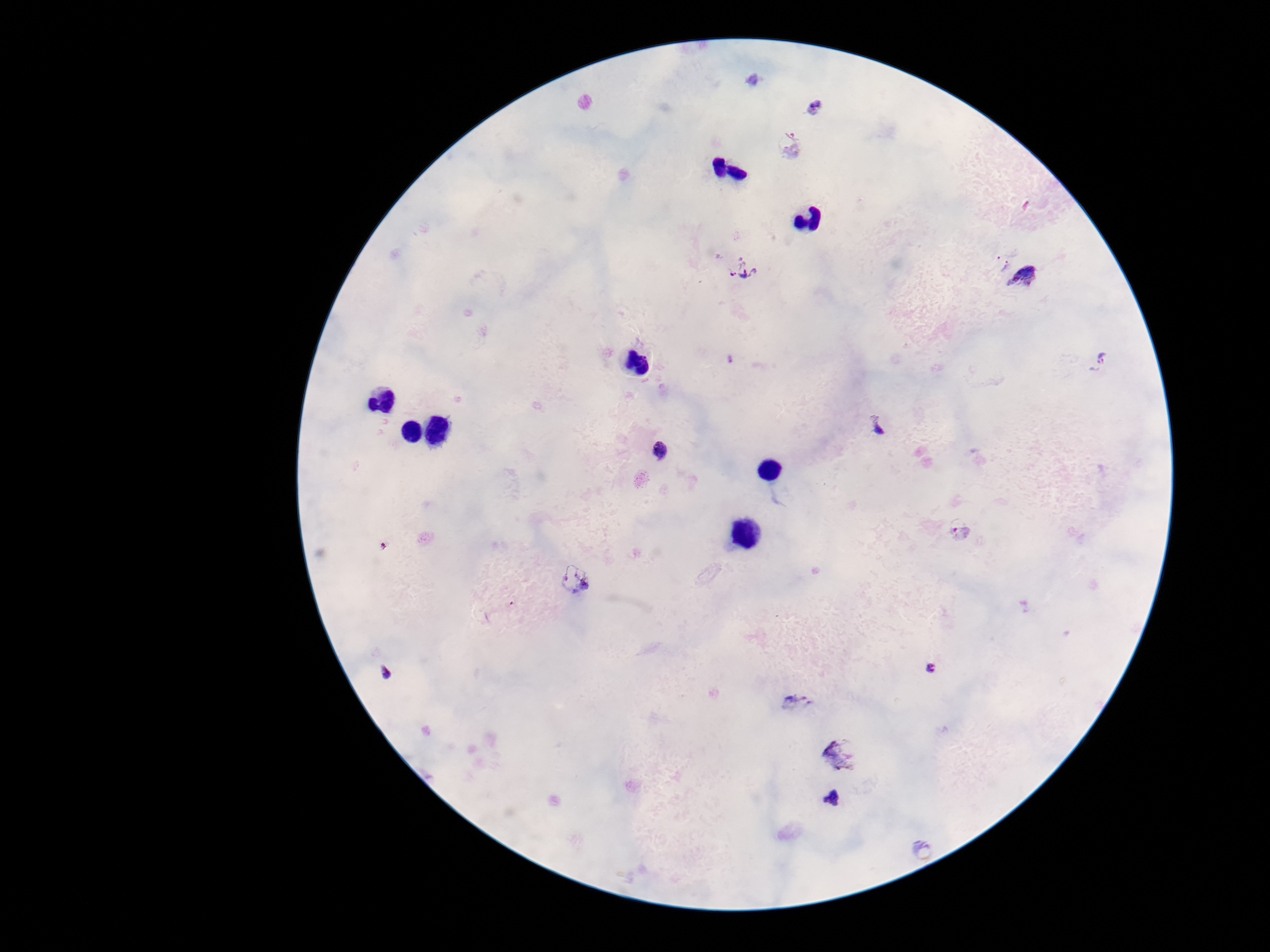
Approximate centers as {x, y} in pixels.
Summary:
  - Plasmodium parasite locations: {752, 82}, {814, 106}, {788, 143}, {998, 260}, {742, 267}, {1026, 277}, {1101, 361}, {877, 426}, {662, 452}, {960, 531}, {575, 579}, {932, 668}, {387, 671}, {794, 705}, {842, 756}, {831, 798}, {922, 851}
  - Stain: Giemsa
  - Capture: smartphone camera through the microscope eyepiece
  - Field of view: single
  - Magnification: 100x
  - Patient malaria status: infected
  - Preparation: thick peripheral-blood smear
  - Image size: 1270×952 pixels